Assess this cell for malaria.
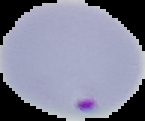

Parasitized.

Summary:
  - Image size: 145×121 pixels
  - Preparation: thin blood film
  - Image type: segmented cell region on a black background